Assess this cell for malaria.
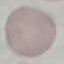

It is uninfected.

Cell patch, automatically extracted from a larger field of view and resized to 64 × 64 pixels. Giemsa-stained preparation. Thin blood smear. Photographed with a smartphone camera at the microscope eyepiece.